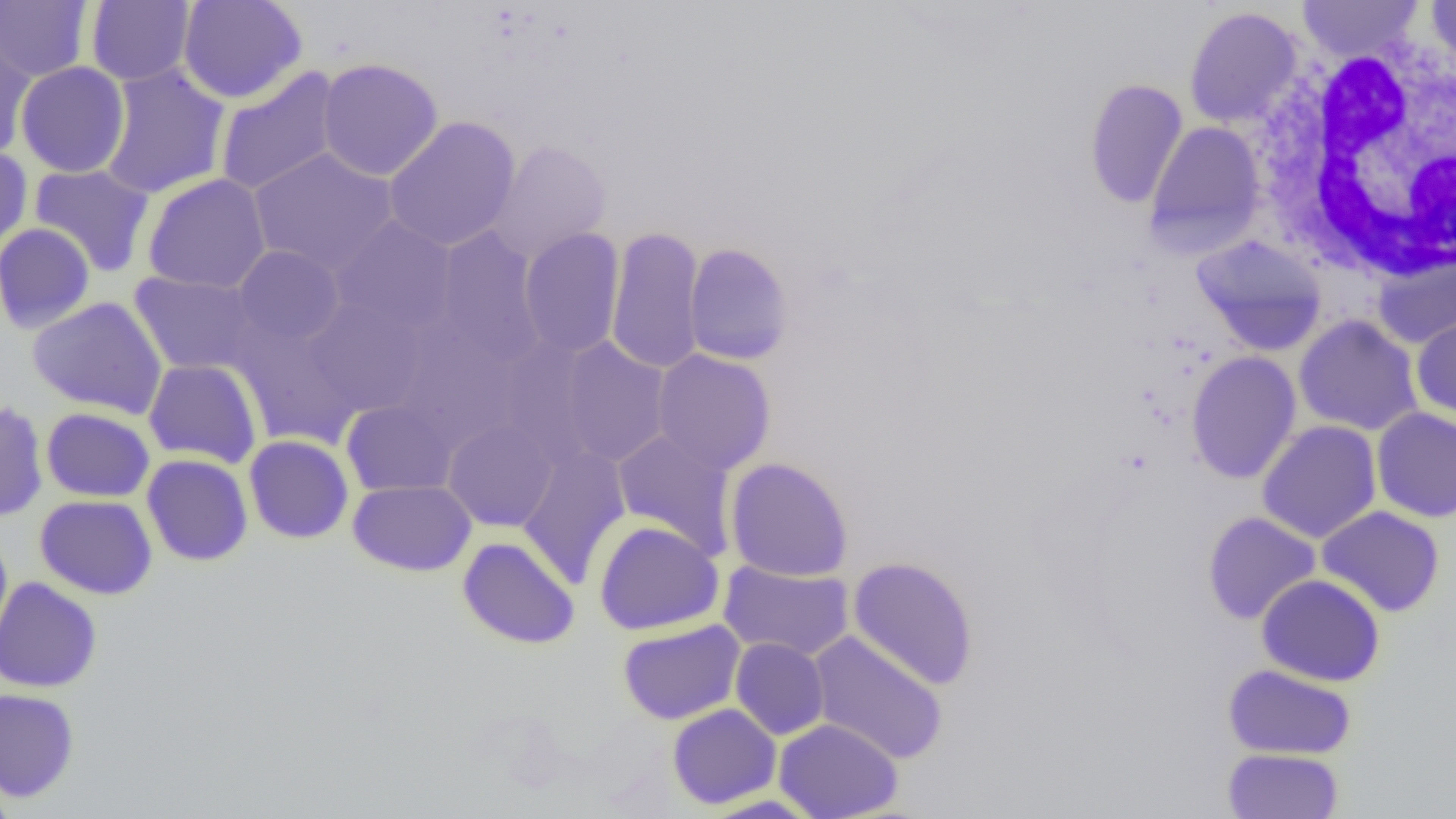

Summary:
  - Coordinate format: approximate bounding boxes as [x1, y1, x2, y2] in pixels
  - Uninfected red blood cell locations: [86, 0, 195, 86], [177, 0, 307, 104], [1297, 0, 1424, 61], [1426, 0, 1456, 75], [0, 1, 94, 81], [1184, 6, 1303, 129], [0, 24, 36, 159], [317, 57, 444, 182], [15, 61, 130, 178], [99, 64, 231, 200], [214, 67, 342, 198], [1083, 78, 1188, 209], [383, 116, 521, 252], [1144, 120, 1266, 256], [487, 139, 612, 263], [0, 147, 33, 253], [248, 147, 400, 277], [29, 164, 155, 277], [142, 173, 272, 294], [330, 215, 458, 336], [0, 222, 96, 334], [432, 226, 546, 366], [605, 226, 706, 374], [519, 227, 625, 358], [1190, 235, 1327, 355], [683, 242, 795, 365], [233, 245, 346, 348], [1373, 252, 1456, 348], [129, 270, 262, 376], [27, 296, 167, 418], [303, 296, 430, 417], [1294, 314, 1424, 436], [1412, 314, 1456, 422], [233, 316, 365, 448], [391, 319, 522, 450], [494, 335, 606, 466], [556, 337, 673, 468], [651, 349, 776, 475], [1186, 351, 1302, 484], [143, 358, 263, 469], [0, 400, 48, 521], [341, 400, 457, 497], [1371, 407, 1456, 523], [41, 408, 155, 502], [443, 419, 558, 531], [1257, 420, 1381, 543], [611, 429, 738, 559], [243, 435, 354, 543], [516, 445, 631, 587], [142, 454, 254, 566], [725, 457, 853, 582], [347, 479, 476, 576], [35, 495, 158, 599], [1317, 506, 1445, 617], [1203, 511, 1320, 625], [594, 520, 724, 635], [0, 530, 13, 653], [457, 536, 580, 649], [847, 556, 979, 690], [718, 560, 854, 661], [1256, 574, 1386, 686], [0, 576, 102, 693], [617, 619, 746, 725], [807, 631, 948, 765], [730, 637, 829, 740], [1222, 664, 1357, 760], [0, 688, 79, 803], [667, 703, 781, 809], [773, 718, 903, 819], [1222, 748, 1343, 819], [0, 772, 16, 819], [698, 793, 824, 818]
  - White blood cell locations: [1254, 40, 1456, 284]
  - Slide-level diagnosis: no evidence of blood parasites
  - Image size: 1456×819 pixels
  - Preparation: thin blood smear
  - Field of view: one of a larger specimen
  - Magnification: 1000x
  - Modality: optical microscopy